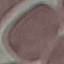
Summary:
  - Result: negative for malaria parasites
  - Image type: cell patch, automatically extracted from a larger field of view and resized to 64 × 64 pixels
  - Preparation: thin smear
  - Capture: smartphone through the microscope eyepiece
  - Stain: Giemsa